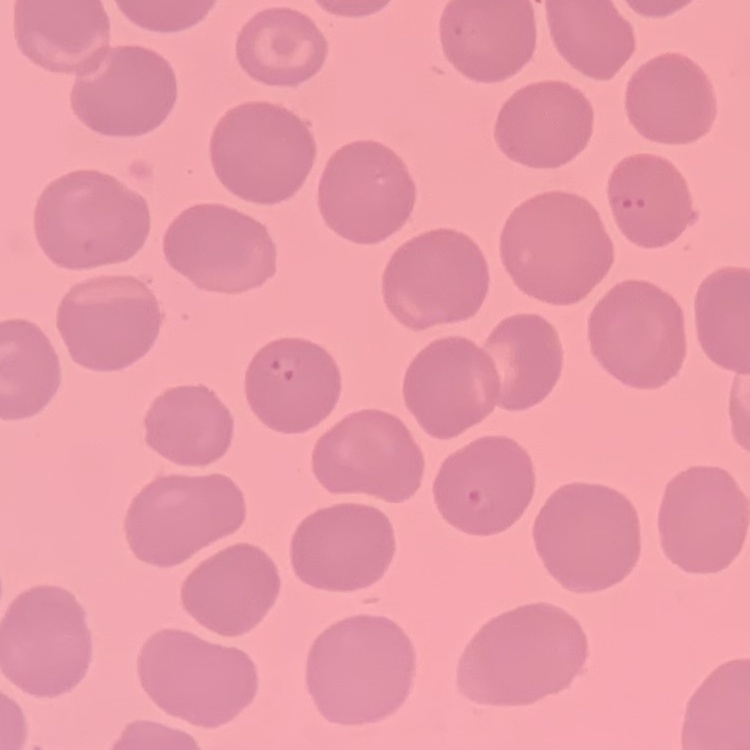 The erythrocytes exhibit no rouleaux formation. Square crop of a larger photomicrograph. Thin peripheral smear. Stained with either Field's or Giemsa.